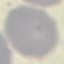 Result: no malaria parasites seen. Giemsa stain. Thin blood film. Cell patch, automatically extracted from a larger field of view and resized to 64 × 64 pixels. Acquired by smartphone through the microscope eyepiece.